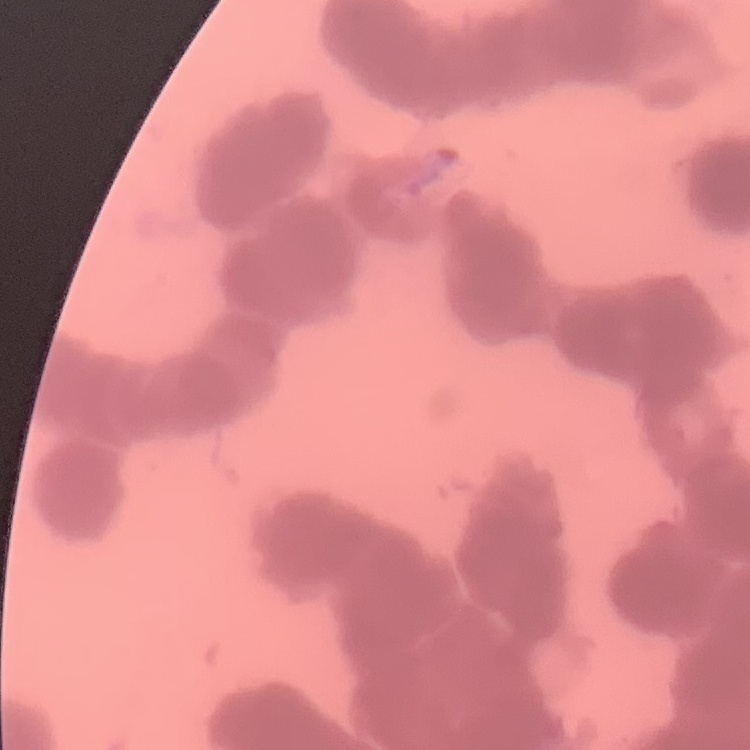

{
  "erythrocyte_morphology": "rouleaux formation",
  "stain": "Field's or Giemsa",
  "image_type": "one tile cut from a larger photomicrograph",
  "preparation": "thin peripheral smear"
}